Name the parasite shown.
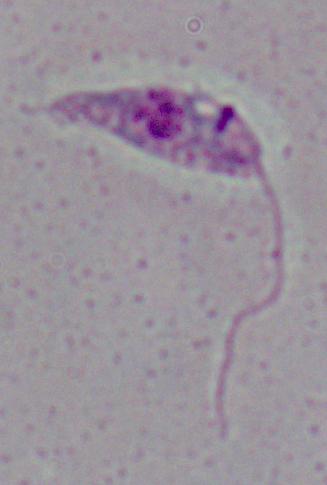

This is Leishmania.

modality = photomicrograph
magnification = 1000x